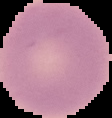

Result: negative for Plasmodium parasites. Image is 112×118 pixels. From a thin blood smear. Cell region segmented out of the field of view; the surrounding area is masked to black.